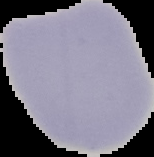 From a thin blood film. Cell region segmented out of the field of view; the surrounding area is masked to black. Image is 154×157 pixels. Malaria status: uninfected.